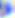
Summary:
  - Modality: photomicrograph
  - Identification: Toxoplasma gondii
  - Magnification: 400x